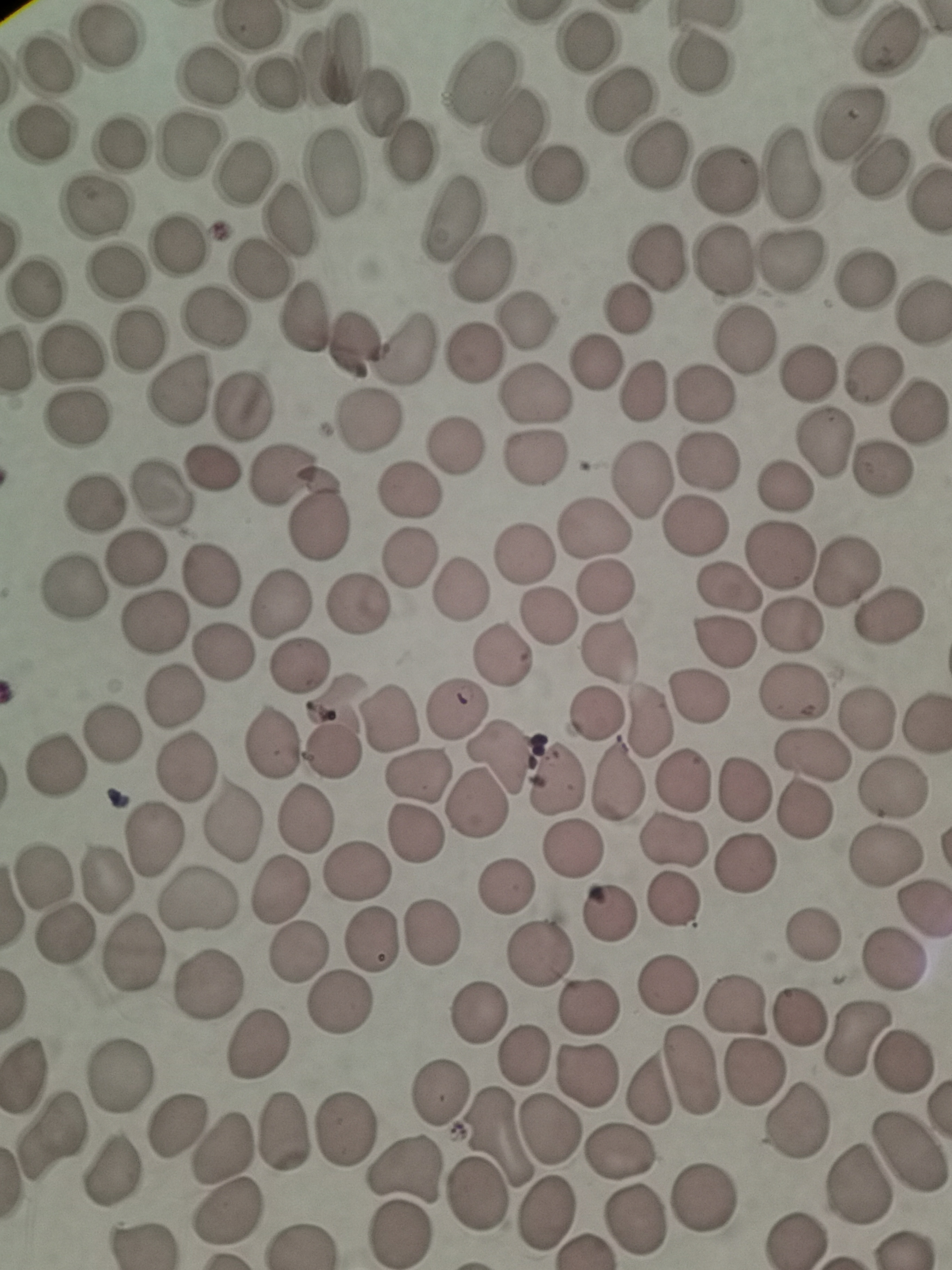

Approximate object centers, in pixels from the top-left corner.
Summary:
  - Cell locations: (x=586, y=40), (x=108, y=41), (x=892, y=41), (x=344, y=59), (x=700, y=60), (x=313, y=67), (x=49, y=68), (x=206, y=77), (x=475, y=78), (x=271, y=86), (x=382, y=99), (x=618, y=99), (x=848, y=118), (x=510, y=127), (x=43, y=132), (x=117, y=142), (x=188, y=143), (x=411, y=152), (x=655, y=159), (x=879, y=171), (x=333, y=172), (x=793, y=172), (x=556, y=174), (x=243, y=176), (x=727, y=182), (x=96, y=210), (x=446, y=221), (x=291, y=222), (x=179, y=243), (x=657, y=257), (x=726, y=260), (x=796, y=261), (x=484, y=267), (x=114, y=269), (x=258, y=271), (x=859, y=283), (x=38, y=290), (x=921, y=310), (x=627, y=311), (x=209, y=316), (x=524, y=320), (x=301, y=321), (x=139, y=336), (x=745, y=340), (x=353, y=345), (x=406, y=346), (x=473, y=352), (x=70, y=357), (x=594, y=366), (x=808, y=375), (x=873, y=377), (x=645, y=388), (x=179, y=389), (x=534, y=393), (x=703, y=396), (x=241, y=404), (x=919, y=411), (x=80, y=420), (x=367, y=421), (x=825, y=442), (x=456, y=444), (x=534, y=457), (x=708, y=461), (x=210, y=468), (x=282, y=471), (x=878, y=472), (x=638, y=478), (x=785, y=485), (x=162, y=495), (x=407, y=495), (x=92, y=507), (x=596, y=525), (x=316, y=527), (x=696, y=527), (x=525, y=553), (x=777, y=555), (x=407, y=558), (x=136, y=560), (x=844, y=571), (x=211, y=575), (x=727, y=586), (x=607, y=587), (x=72, y=588), (x=461, y=589), (x=275, y=606), (x=358, y=606), (x=889, y=614), (x=546, y=615), (x=154, y=624), (x=790, y=625), (x=729, y=642), (x=221, y=652), (x=608, y=652), (x=502, y=655), (x=298, y=667), (x=174, y=691), (x=794, y=693), (x=701, y=697), (x=337, y=705), (x=454, y=709), (x=595, y=716), (x=650, y=717), (x=389, y=719), (x=866, y=719), (x=114, y=735), (x=272, y=743), (x=332, y=753), (x=808, y=754), (x=501, y=756), (x=54, y=763), (x=182, y=767), (x=419, y=774), (x=555, y=780), (x=618, y=781), (x=679, y=782), (x=893, y=785), (x=743, y=792), (x=801, y=808), (x=474, y=809), (x=305, y=820), (x=230, y=822), (x=417, y=831), (x=154, y=843), (x=671, y=845), (x=569, y=848), (x=883, y=858), (x=742, y=864), (x=357, y=867), (x=42, y=872), (x=106, y=879), (x=505, y=885), (x=280, y=893), (x=204, y=901), (x=674, y=902), (x=922, y=911), (x=609, y=914), (x=433, y=931), (x=61, y=937), (x=811, y=940), (x=373, y=942), (x=136, y=953), (x=295, y=953), (x=541, y=956), (x=894, y=964), (x=205, y=981), (x=667, y=985), (x=342, y=1002), (x=588, y=1006), (x=736, y=1007), (x=480, y=1015), (x=797, y=1017), (x=858, y=1039), (x=261, y=1045), (x=524, y=1057), (x=907, y=1063), (x=28, y=1071), (x=692, y=1071), (x=121, y=1072), (x=752, y=1072), (x=590, y=1075), (x=647, y=1088), (x=441, y=1092), (x=797, y=1120), (x=175, y=1121), (x=282, y=1128), (x=551, y=1130), (x=344, y=1131), (x=51, y=1133), (x=500, y=1133), (x=221, y=1148), (x=618, y=1150), (x=909, y=1154), (x=404, y=1167), (x=112, y=1168), (x=862, y=1187), (x=478, y=1196), (x=705, y=1196), (x=224, y=1209), (x=549, y=1211), (x=637, y=1220), (x=398, y=1235), (x=793, y=1239)
  - Field of view: single
  - Image size: 952×1270 pixels
  - Stain: Giemsa
  - Capture: smartphone through the microscope eyepiece
  - Preparation: thin blood film